Report the malaria status of this cell.
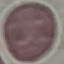
It is uninfected.

Summary:
  - Capture: smartphone through the microscope eyepiece
  - Stain: Giemsa
  - Image type: automatically extracted cell patch, resized to 64 × 64 pixels
  - Preparation: thin smear